Locate and identify every blood parasite.
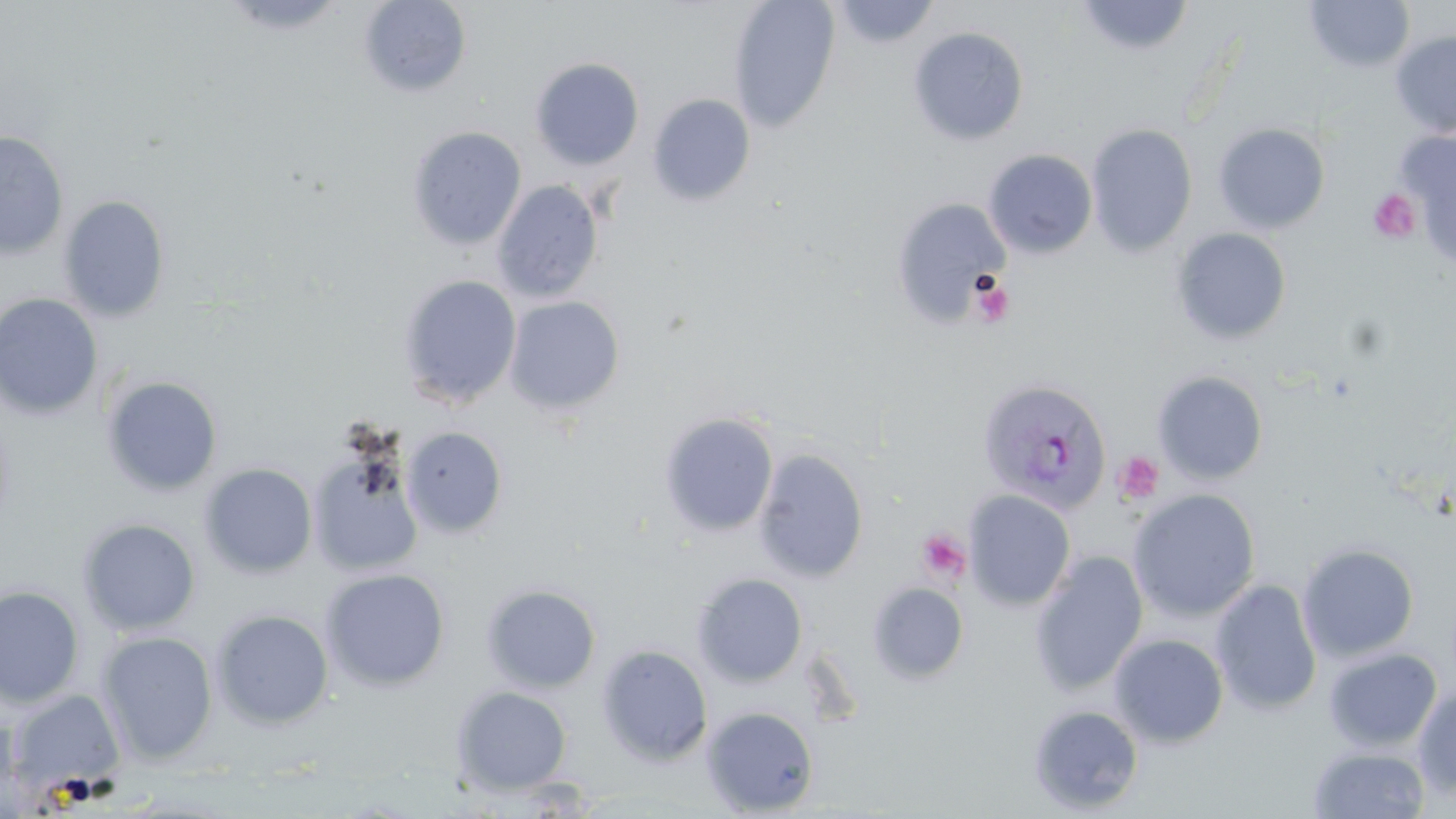

Approximate bounding boxes as (x1,y1)-(x2,y2) corner pairs in pixels.
Plasmodium vivax-infected red blood cells: (976,377)-(1112,514).
No Plasmodium falciparum, Plasmodium ovale, Plasmodium malariae, Babesia divergens, or Trypanosoma brucei observed.

Summary:
  - Uninfected red blood cell locations: (219,0)-(349,35), (358,0)-(472,97), (728,0)-(841,134), (1075,0)-(1196,58), (1303,0)-(1416,74), (828,1)-(942,48), (908,26)-(1029,145), (1390,30)-(1456,138), (530,57)-(645,170), (648,94)-(756,206), (1086,123)-(1198,257), (1213,123)-(1330,234), (407,126)-(526,250), (1397,130)-(1456,268), (0,131)-(69,259), (983,148)-(1098,259), (492,180)-(604,303), (58,195)-(170,322), (891,197)-(1010,327), (1172,227)-(1291,345), (398,276)-(521,409), (0,293)-(103,420), (503,295)-(625,416), (1152,370)-(1269,485), (101,375)-(223,497), (659,413)-(779,537), (401,426)-(508,539), (753,448)-(869,582), (310,450)-(424,576), (199,463)-(318,579), (1127,488)-(1261,622), (963,490)-(1076,610), (77,517)-(201,635), (1297,542)-(1420,662), (1029,550)-(1149,696), (320,568)-(450,691), (692,573)-(808,687), (1210,579)-(1323,716), (867,582)-(969,684), (481,583)-(602,693), (0,584)-(85,709), (211,609)-(333,729), (97,630)-(218,764), (1109,633)-(1229,748), (596,644)-(713,765), (1323,647)-(1443,752), (451,686)-(573,795), (1413,686)-(1456,799), (8,690)-(126,795), (1028,703)-(1144,815), (701,706)-(819,816), (1308,745)-(1431,818)
  - Platelet locations: (1395,143)-(1456,253), (1368,189)-(1420,242), (971,275)-(1015,329), (1114,451)-(1164,503), (918,528)-(971,584)
  - Slide-level diagnosis: Plasmodium vivax
  - Magnification: 1000x
  - Modality: light microscopy
  - Stain: May-Grünwald-Giemsa
  - Preparation: thin blood smear
  - Field of view: single
  - Image size: 1456×819 pixels